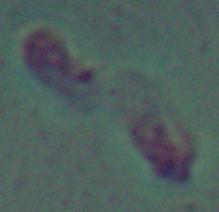

Summary:
  - Magnification: 1000x
  - Identification: Leishmania
  - Modality: micrograph